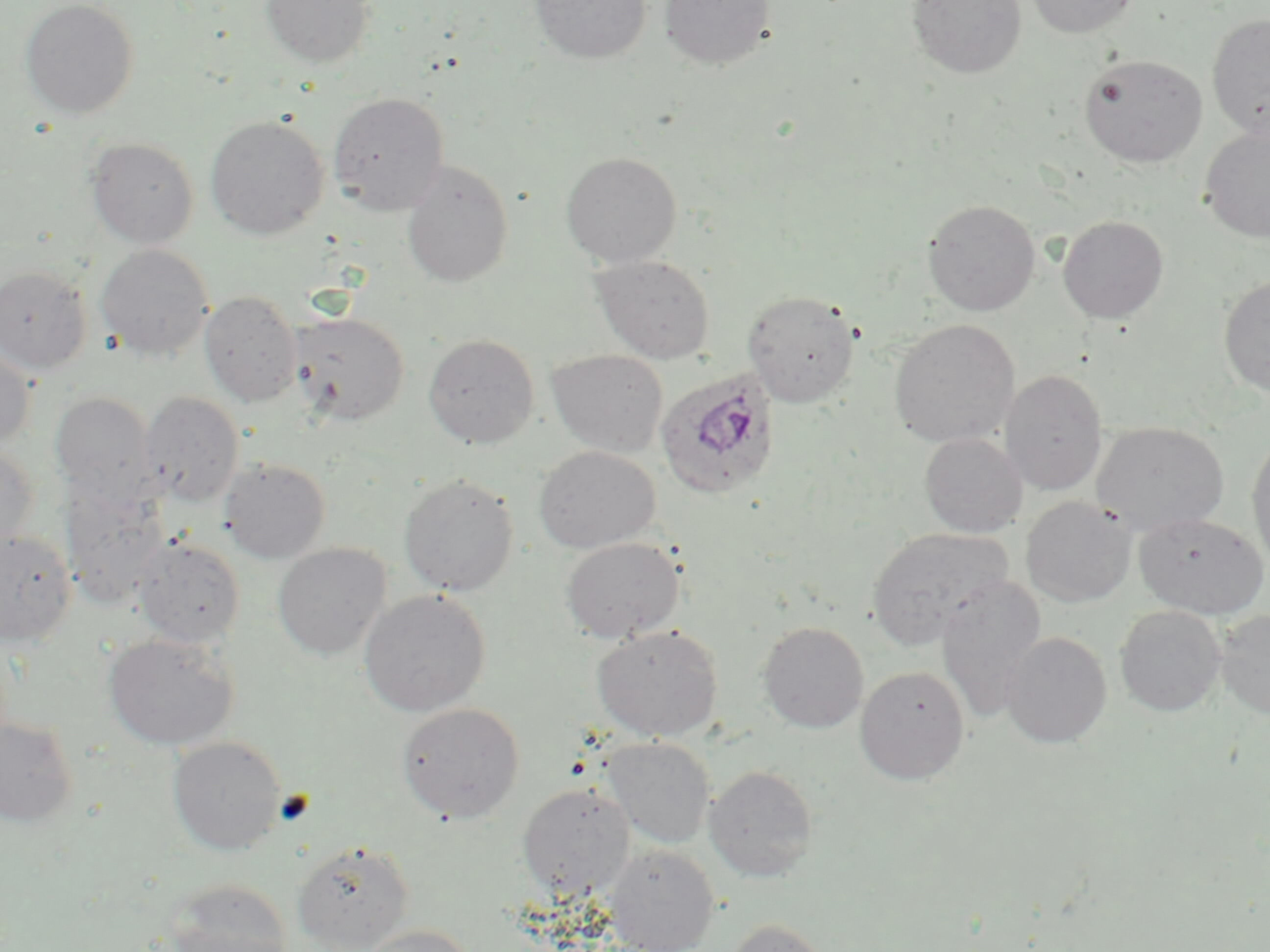
slide_level_diagnosis: Plasmodium ovale
uninfected_red_blood_cell_locations: 'approximate bounding boxes as [x1, y1, x2, y2] in pixels: [19, 0, 139, 119], [260, 0, 376, 68], [530, 0, 651, 64], [659, 0, 776, 70], [906, 0, 1027, 80], [1024, 0, 1140, 38], [1207, 13, 1270, 142], [1078, 54, 1208, 167], [328, 91, 450, 215], [205, 115, 329, 240], [1199, 124, 1270, 244], [85, 137, 200, 248], [560, 151, 682, 267], [401, 160, 514, 287], [922, 199, 1041, 315], [1057, 215, 1169, 324], [95, 244, 214, 361], [589, 253, 716, 364], [0, 266, 92, 373], [1218, 274, 1270, 399], [742, 289, 861, 407], [198, 290, 303, 407], [289, 311, 410, 426], [889, 319, 1020, 448], [423, 333, 540, 448], [0, 345, 35, 449], [546, 348, 669, 457], [1000, 370, 1108, 494], [139, 390, 244, 507], [49, 391, 157, 507], [1091, 420, 1230, 537], [918, 432, 1028, 538], [1246, 434, 1270, 570], [0, 444, 39, 554], [533, 445, 660, 553], [218, 458, 331, 563], [398, 474, 519, 596], [59, 479, 171, 607], [1020, 496, 1136, 607], [1133, 512, 1268, 618], [865, 527, 1013, 651], [0, 528, 77, 646], [132, 536, 245, 648], [560, 537, 684, 643], [272, 543, 391, 660], [935, 574, 1047, 719], [359, 588, 491, 717], [1114, 605, 1226, 716], [1215, 609, 1270, 719], [758, 621, 869, 733], [591, 625, 723, 741], [102, 632, 240, 751], [1000, 632, 1112, 747], [854, 665, 970, 785], [396, 702, 524, 823], [0, 716, 79, 826], [167, 736, 286, 855], [602, 737, 714, 849], [703, 765, 819, 882], [517, 783, 635, 898], [292, 840, 414, 951], [605, 844, 719, 952], [160, 879, 293, 952], [724, 918, 835, 952], [359, 925, 474, 952]'
stain: May-Grünwald-Giemsa
magnification: 1000x
preparation: thin blood film
platelet_locations: 'approximate bounding boxes as [x1, y1, x2, y2] in pixels: [275, 791, 316, 826]'
field_of_view: single
plasmodium_ovale_infected_red_blood_cell_locations: 'approximate bounding boxes as [x1, y1, x2, y2] in pixels: [654, 366, 782, 501]'
modality: optical microscopy
image_size: 1270×952 pixels